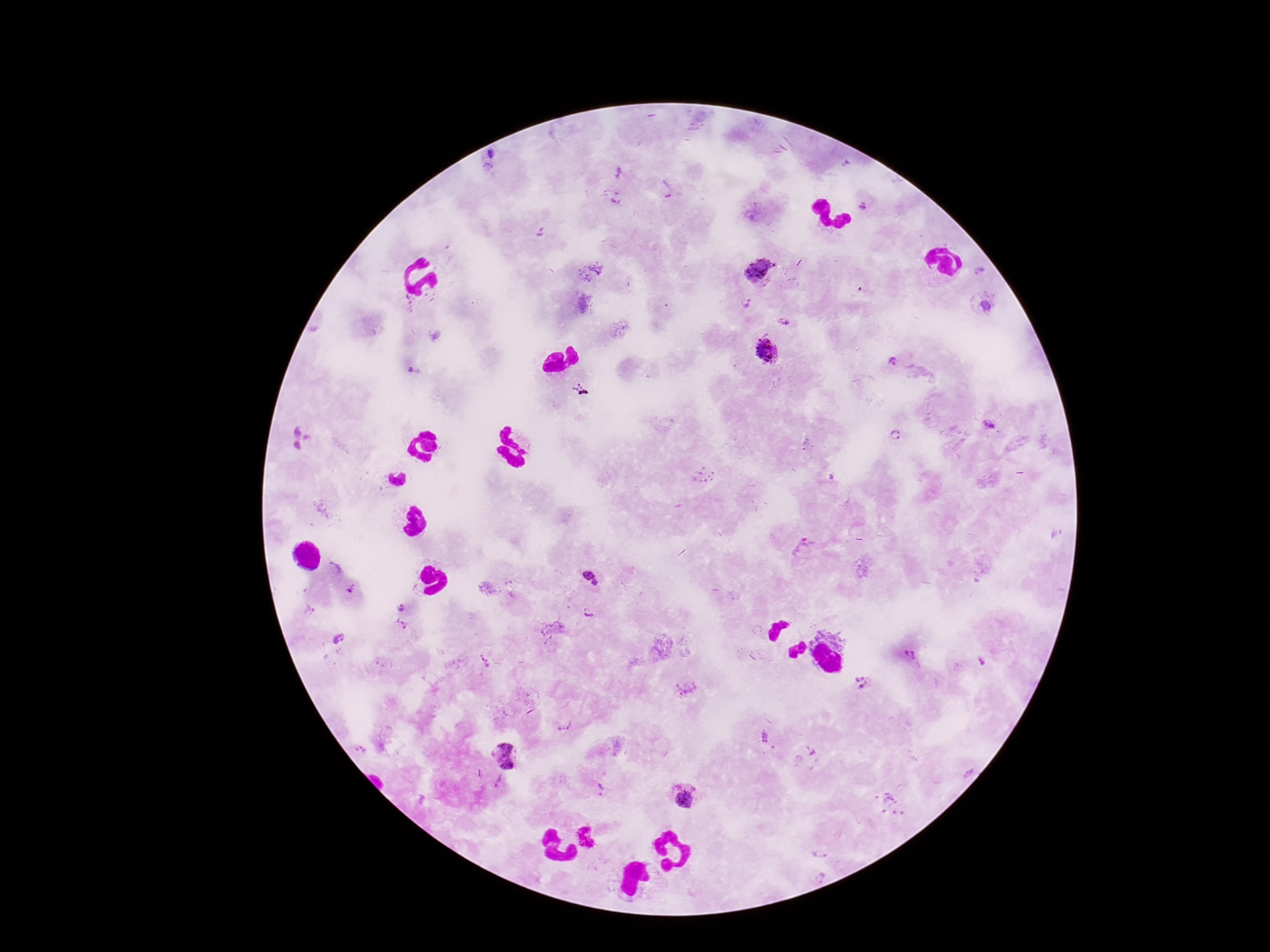
stain = Giemsa
patient malaria status = infected
image size = 1270×952 pixels
magnification = 100x
Plasmodium parasite locations = approximate object centers, in pixels from the top-left corner: (x=492, y=154), (x=488, y=167), (x=617, y=173), (x=666, y=188), (x=616, y=197), (x=865, y=204), (x=539, y=233), (x=590, y=271), (x=979, y=271), (x=759, y=272), (x=747, y=304), (x=987, y=306), (x=784, y=321), (x=766, y=350), (x=897, y=366), (x=413, y=372), (x=581, y=391), (x=988, y=424), (x=295, y=432), (x=896, y=436), (x=307, y=437), (x=297, y=445), (x=805, y=550), (x=334, y=569), (x=588, y=574), (x=596, y=583), (x=353, y=590), (x=402, y=608), (x=310, y=609), (x=590, y=613), (x=402, y=624), (x=339, y=638), (x=911, y=656), (x=485, y=661), (x=980, y=662), (x=861, y=682), (x=765, y=737), (x=774, y=748), (x=361, y=749), (x=811, y=751), (x=506, y=756), (x=499, y=782), (x=599, y=790), (x=686, y=797), (x=889, y=804), (x=820, y=852), (x=821, y=876)
preparation = thick blood film
capture = smartphone camera through the microscope eyepiece
field of view = one from this slide